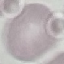

{
  "malaria_status": "uninfected",
  "preparation": "thin blood smear",
  "capture": "smartphone through the microscope eyepiece",
  "stain": "Giemsa",
  "image_type": "cell patch, automatically extracted from a larger field of view and resized to 64 × 64 pixels"
}